Classify the preparation.
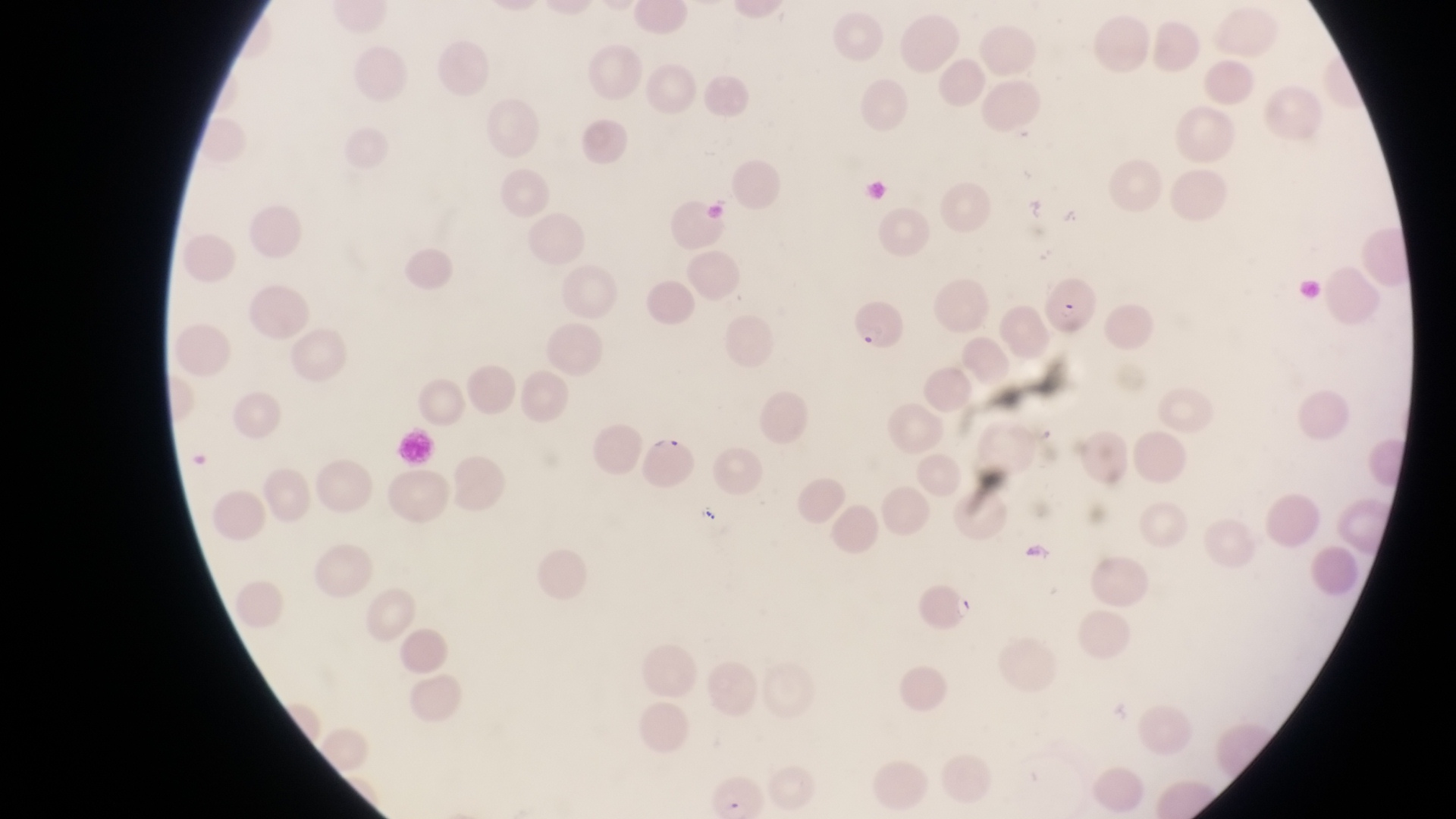
Thin blood smear.

Approximate bounding boxes as (left, top, right, bottom) in pixels.
Summary:
  - Trophozoite locations: (952, 594, 979, 624)
  - Parasitised red blood cell locations: (1043, 267, 1099, 331), (848, 298, 901, 354), (644, 429, 702, 495)
  - Magnification: 1000x
  - Field of view: single
  - Country: Uganda
  - Image size: 1456×819 pixels
  - Capture: smartphone photograph through the eyepiece of an Olympus CX-23 microscope